Classify this cell by malaria status.
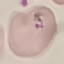

It is parasitized.

{
  "stain": "Giemsa",
  "preparation": "thin blood smear",
  "capture": "smartphone camera at the microscope eyepiece",
  "image_type": "cell patch, automatically extracted from a larger field of view and resized to 64 × 64 pixels"
}